Report the malaria status of this cell.
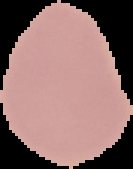
It is uninfected.

Image is 133×169 pixels. From a thin blood film. Segmented cell region on a black background.